Assess this cell for malaria.
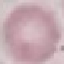

Uninfected.

Acquired by smartphone through the microscope eyepiece. Cell patch, automatically extracted from a larger field of view and resized to 64 × 64 pixels. Giemsa stain. Thin blood film.